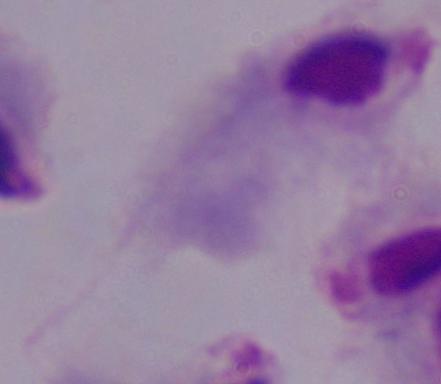
A trichomonad is shown. 1000x magnification. Photomicrograph.